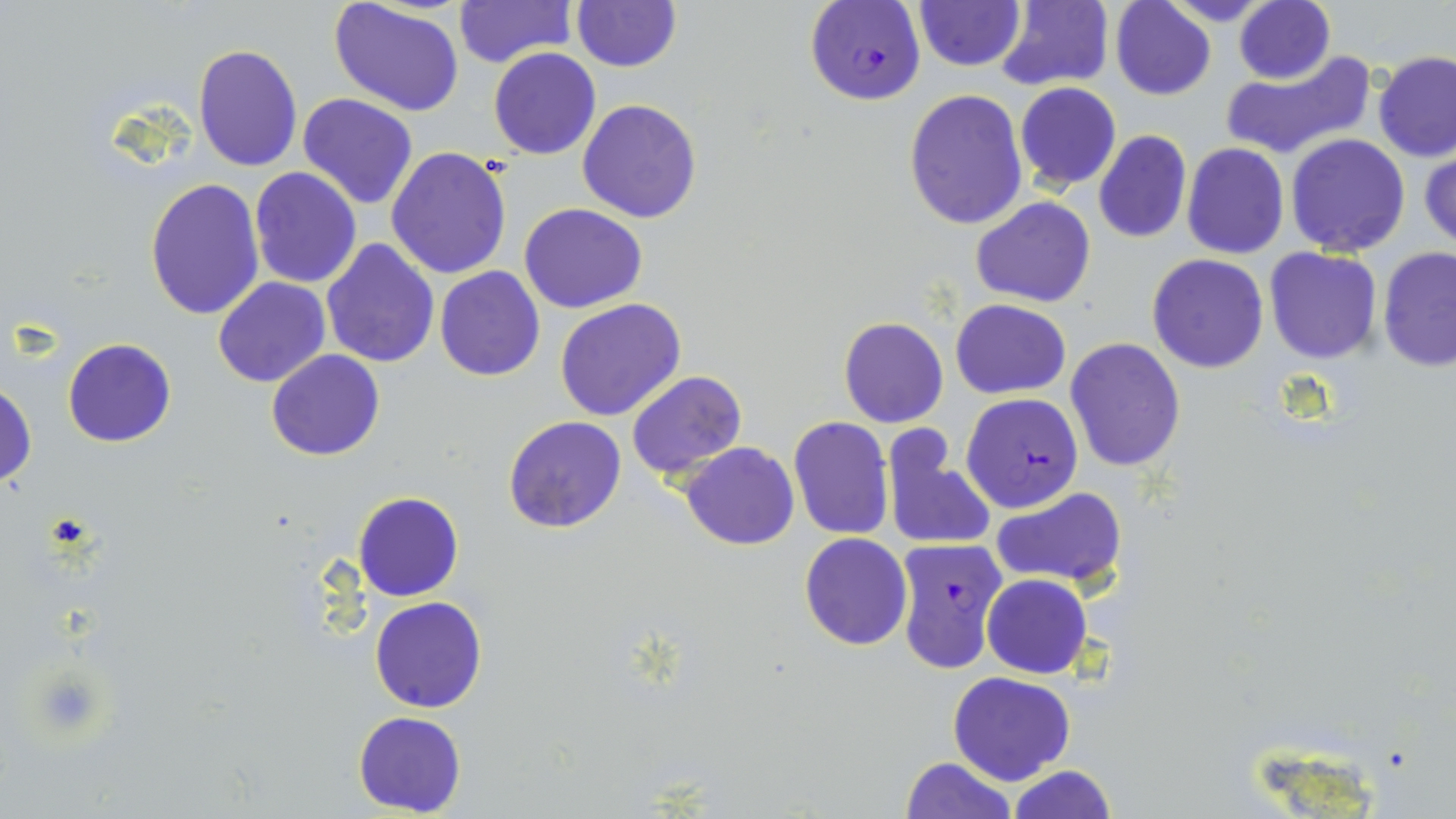

Approximate bounding boxes as [x1, y1, x2, y2] in pixels. Plasmodium falciparum-infected red blood cell locations: [805, 1, 926, 106], [961, 393, 1083, 513], [892, 536, 1008, 674]. Uninfected red blood cell locations: [914, 0, 1024, 70], [1109, 0, 1217, 100], [1160, 0, 1275, 27], [1234, 0, 1335, 85], [451, 1, 577, 68], [571, 1, 682, 73], [328, 2, 467, 117], [992, 2, 1114, 90], [192, 42, 303, 172], [488, 47, 601, 160], [1220, 48, 1375, 161], [1373, 51, 1455, 162], [1014, 82, 1122, 191], [904, 90, 1029, 231], [297, 92, 418, 209], [578, 98, 704, 222], [1092, 130, 1192, 243], [1285, 133, 1412, 256], [1182, 144, 1289, 259], [386, 147, 513, 281], [1420, 147, 1455, 253], [248, 167, 362, 288], [145, 178, 265, 323], [971, 195, 1094, 308], [520, 203, 648, 314], [321, 238, 440, 368], [1263, 247, 1382, 365], [1378, 247, 1456, 373], [1148, 255, 1269, 373], [435, 266, 546, 381], [212, 277, 331, 388], [555, 298, 688, 422], [951, 300, 1071, 398], [838, 316, 949, 428], [63, 337, 176, 447], [1064, 337, 1185, 473], [265, 349, 385, 461], [626, 369, 747, 480], [1, 381, 36, 490], [503, 415, 627, 534], [788, 415, 895, 540], [880, 425, 996, 552], [679, 443, 800, 549], [992, 486, 1127, 590], [353, 491, 464, 602], [798, 532, 912, 650], [981, 574, 1092, 678], [370, 596, 487, 713], [948, 671, 1075, 786], [352, 711, 467, 816], [900, 757, 1017, 818], [1006, 765, 1117, 819]. Slide-level diagnosis: Plasmodium falciparum. Light microscopy. Image is 1456×819 pixels. Thin blood film. May-Grünwald-Giemsa stain. One field of a larger specimen. Captured at 1000x magnification.